Locate platelets.
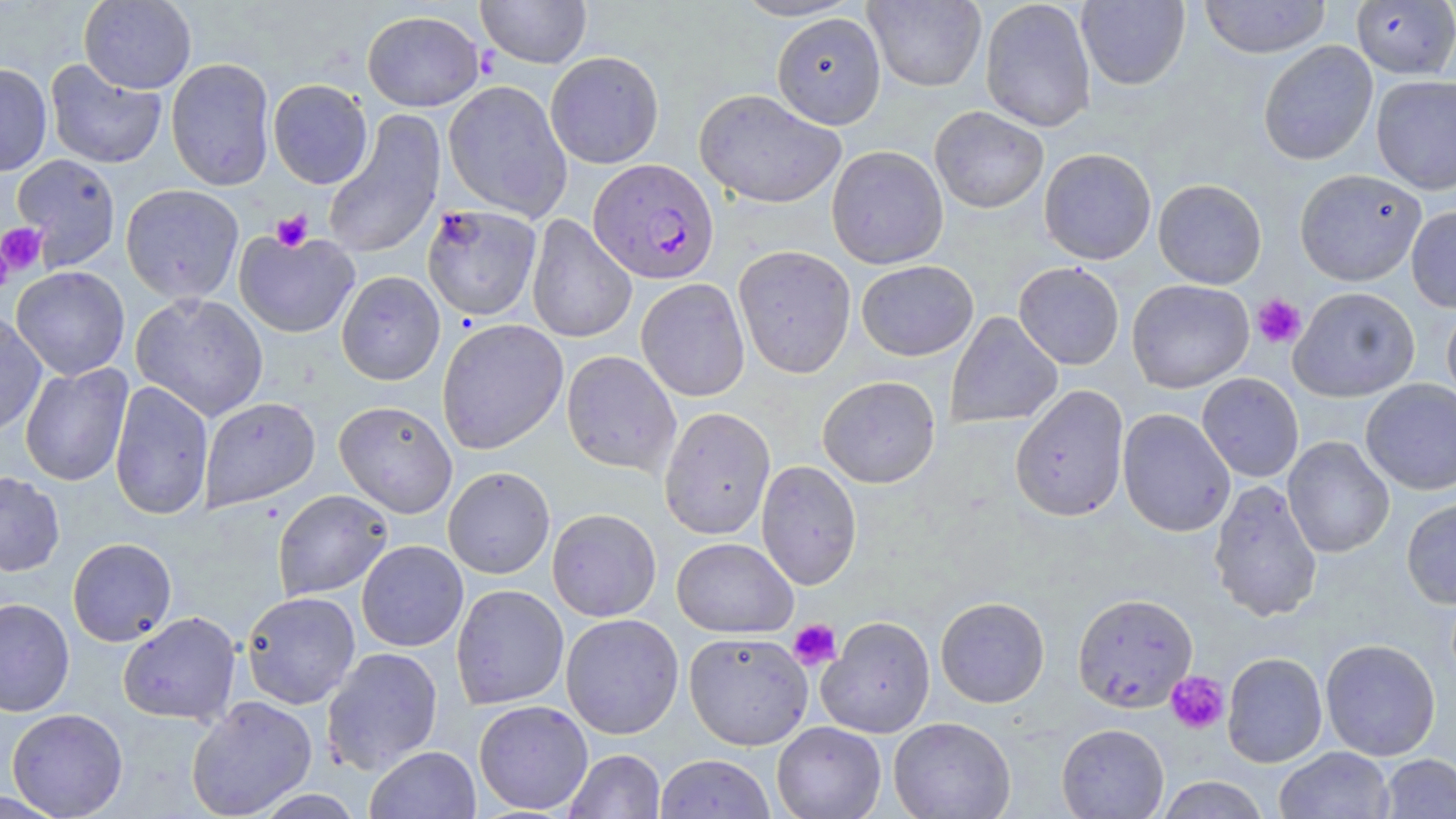
Approximate bounding boxes as [x1, y1, x2, y2] in pixels.
Platelets: [271, 210, 313, 251], [0, 222, 48, 278], [0, 245, 13, 296], [1251, 294, 1306, 349], [788, 619, 841, 671], [1165, 671, 1229, 734].

{
  "slide_level_diagnosis": "Plasmodium falciparum",
  "image_size": "1456×819 pixels",
  "field_of_view": "one of a larger specimen",
  "preparation": "thin blood film",
  "magnification": "1000x",
  "uninfected_red_blood_cell_locations": "approximate bounding boxes as [x1, y1, x2, y2] in pixels: [79, 0, 197, 94], [476, 0, 592, 68], [729, 0, 864, 21], [864, 0, 987, 92], [980, 0, 1096, 133], [1076, 0, 1190, 90], [1199, 0, 1331, 59], [1350, 1, 1456, 79], [362, 10, 485, 111], [771, 13, 886, 129], [1258, 40, 1378, 166], [545, 51, 664, 169], [166, 58, 276, 191], [45, 59, 167, 169], [0, 62, 52, 176], [1371, 75, 1456, 195], [268, 79, 373, 189], [443, 81, 572, 221], [694, 88, 847, 209], [929, 105, 1049, 213], [322, 111, 446, 260], [826, 145, 948, 269], [1038, 148, 1157, 265], [12, 154, 121, 269], [1294, 169, 1427, 286], [1153, 179, 1267, 289], [120, 183, 244, 304], [421, 204, 542, 322], [1406, 205, 1456, 313], [526, 214, 637, 344], [233, 230, 360, 339], [732, 245, 856, 378], [856, 260, 978, 361], [1013, 261, 1125, 370], [11, 266, 130, 381], [336, 270, 445, 386], [636, 278, 750, 402], [1126, 279, 1254, 393], [1289, 286, 1420, 402], [130, 292, 269, 422], [1441, 301, 1456, 408], [0, 311, 47, 438], [945, 311, 1063, 429], [436, 318, 568, 454], [561, 350, 681, 477], [20, 362, 134, 487], [1197, 373, 1304, 482], [817, 375, 941, 488], [1360, 379, 1456, 495], [109, 380, 214, 521], [1010, 385, 1129, 522], [199, 397, 321, 512], [333, 401, 458, 518], [659, 406, 776, 540], [1117, 409, 1235, 538], [1282, 436, 1395, 558], [756, 460, 862, 590], [443, 466, 555, 579], [0, 471, 65, 576], [1208, 479, 1323, 622], [273, 489, 393, 601], [1401, 497, 1456, 609], [547, 508, 662, 622], [67, 537, 177, 646], [671, 537, 798, 637], [356, 540, 468, 651], [451, 584, 569, 709], [241, 591, 361, 709], [1072, 593, 1198, 713], [935, 596, 1050, 708], [0, 597, 75, 717], [118, 611, 241, 726], [560, 613, 684, 739], [817, 615, 936, 738], [683, 631, 813, 750], [1320, 638, 1441, 761], [321, 647, 443, 774], [1222, 652, 1327, 768], [186, 696, 318, 819], [473, 700, 593, 815], [6, 708, 128, 818], [888, 717, 1016, 818], [772, 721, 886, 819], [1057, 723, 1169, 818], [365, 746, 481, 819], [1274, 746, 1395, 819], [564, 749, 665, 818], [1378, 753, 1456, 818], [655, 754, 775, 819], [1155, 776, 1271, 818], [0, 789, 66, 819]",
  "modality": "light microscopy",
  "stain": "May-Grünwald-Giemsa",
  "plasmodium_falciparum_infected_red_blood_cell_locations": "approximate bounding boxes as [x1, y1, x2, y2] in pixels: [588, 158, 719, 284]"
}